Locate every Plasmodium parasite and identify its life-cycle stage.
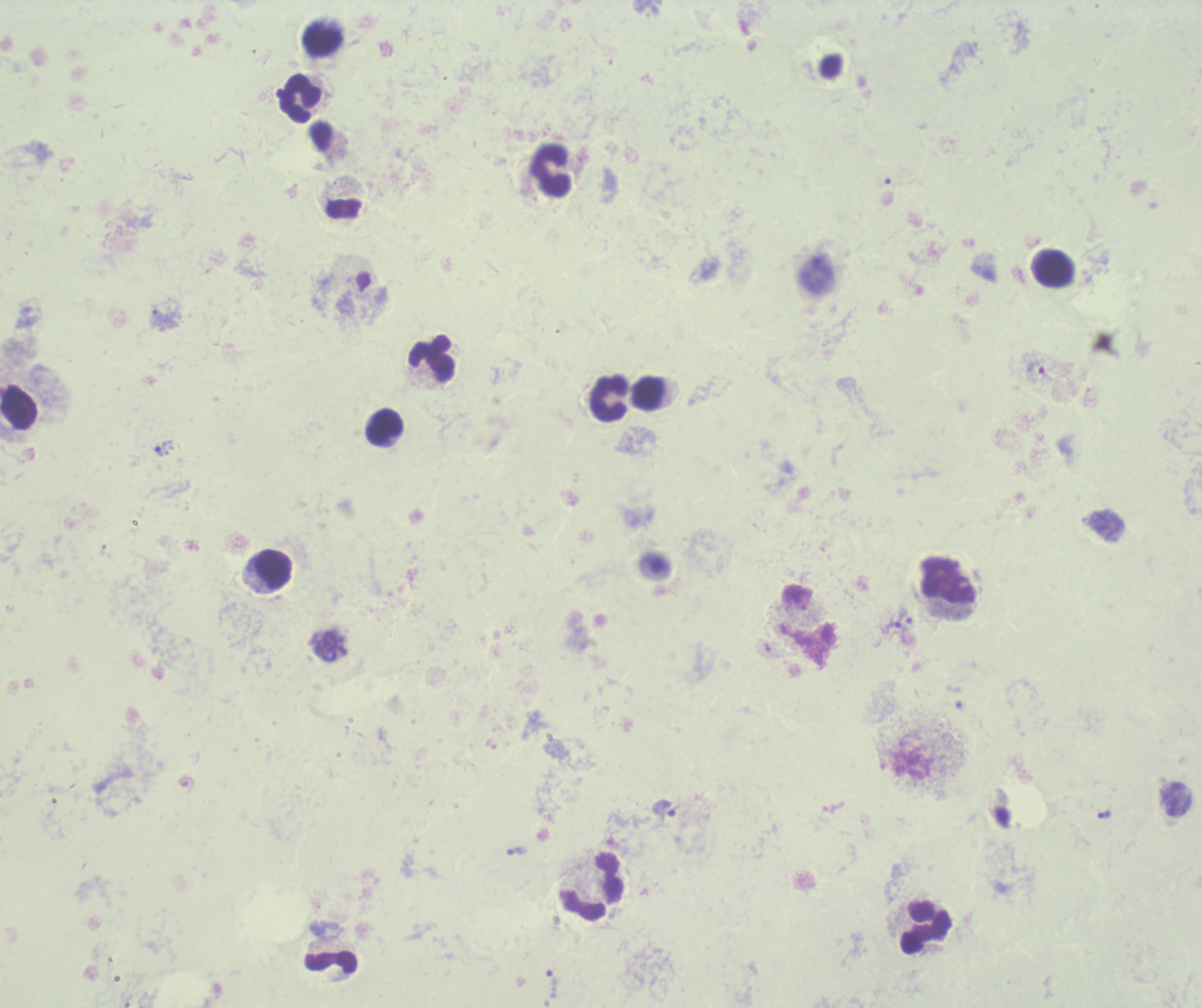

Approximate centers as [x, y] in pixels.
Trophozoites: [1037, 372], [163, 446], [900, 617], [663, 809], [1104, 814], [516, 851], [552, 984].
Schizonts: [331, 646].
No gametocyte forms observed.

Approximate centers as [x, y] in pixels. Leukocyte locations: [324, 38], [301, 99], [551, 170], [344, 209], [1055, 269], [432, 357], [649, 394], [610, 399], [384, 427], [273, 569], [949, 582], [592, 886], [925, 927], [331, 961]. Thick blood smear. Image is 1202×1008 pixels. Background quality: unsatisfactory. Single field of view. Romanowsky stain. Previously used in an actual diagnosis. Captured at 100x magnification.